Assess this cell for malaria.
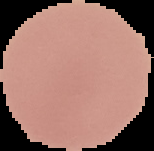
Uninfected.

preparation: thin blood smear
image_size: 154×151 pixels
image_type: segmented cell region with the area outside set to black